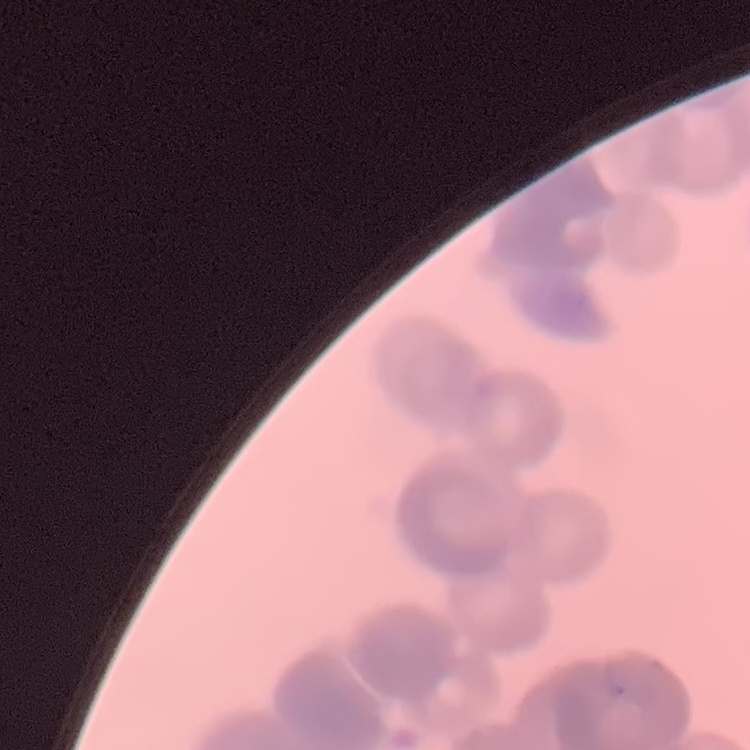
red_blood_cell_morphology: rouleaux formation
stain: Field's or Giemsa
preparation: thin peripheral smear
image_type: square crop of a larger photomicrograph